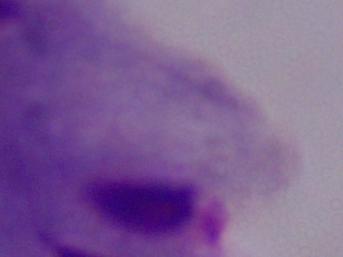

{
  "identification": "trichomonad",
  "modality": "photomicrograph",
  "magnification": "1000x"
}